Assess for malaria.
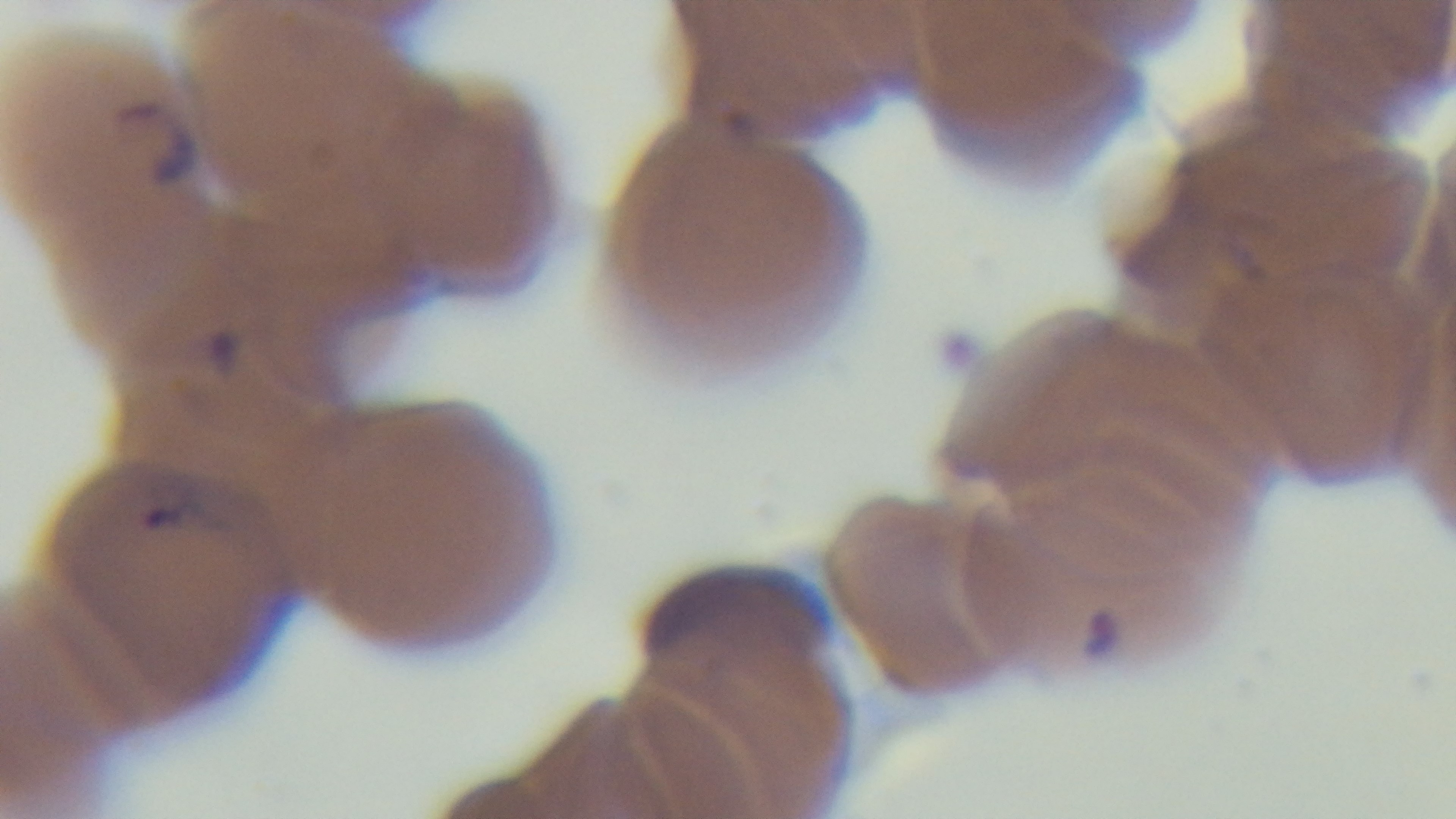

Infected.

Summary:
  - Modality: light microscopy
  - Capture: mounted 4K digital camera
  - Field of view: one from the slide
  - Preparation: thin
  - Objective: 100x oil immersion
  - Stain: Giemsa